State the preparation type.
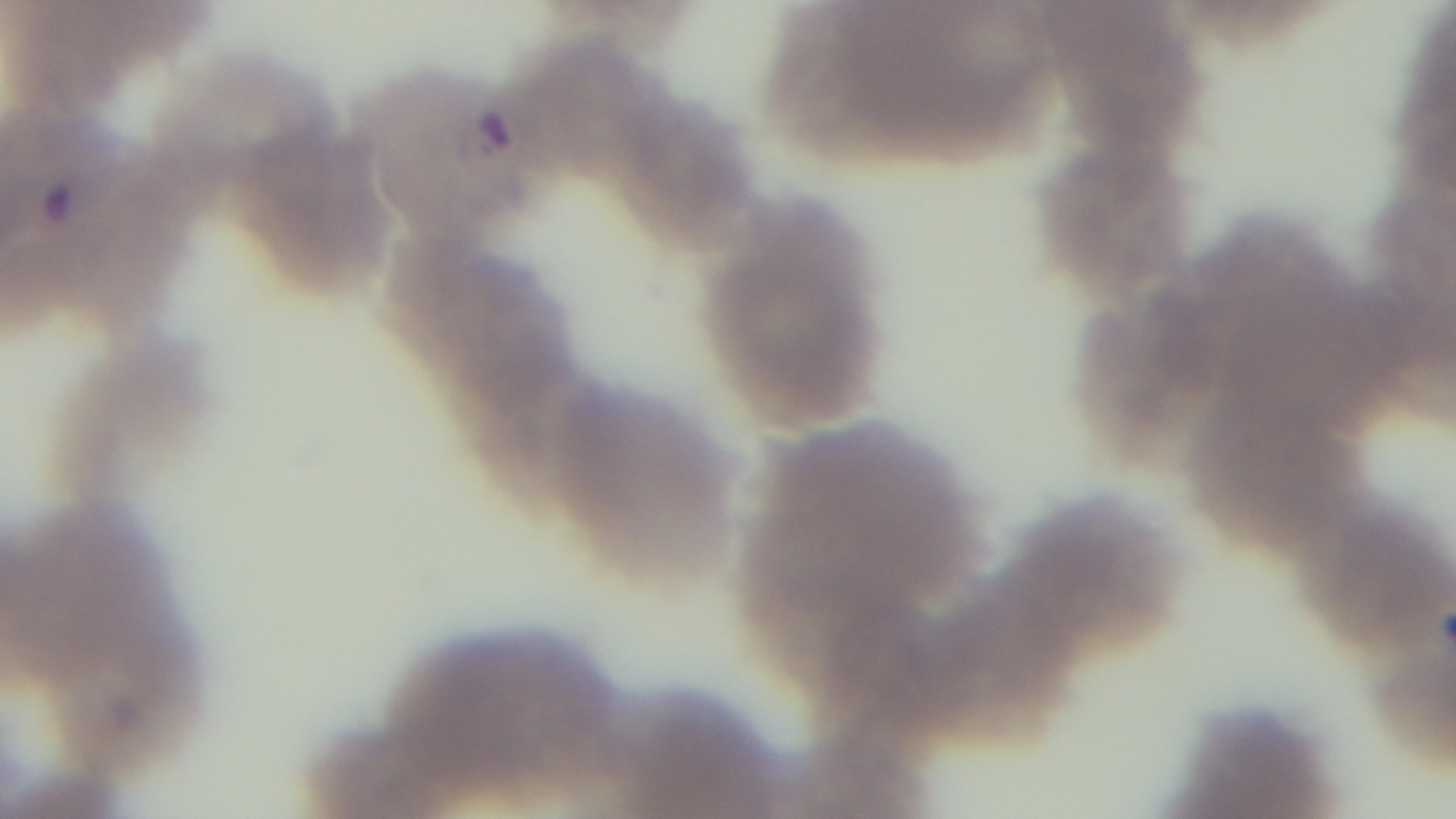

A thin smear.

field_of_view: single
capture: mounted 4K digital camera
objective: 100x oil immersion
modality: light microscopy
stain: Giemsa
malaria_status: positive